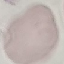
Summary:
  - Malaria status: uninfected
  - Stain: Giemsa
  - Preparation: thin blood smear
  - Image type: cell patch, automatically extracted from a larger field of view and resized to 64 × 64 pixels
  - Capture: smartphone through the microscope eyepiece